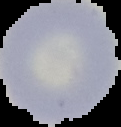

Summary:
  - Image size: 121×127 pixels
  - Preparation: thin blood smear
  - Malaria status: uninfected
  - Image type: segmented cell region with the area outside set to black